Locate every Plasmodium parasite and every leukocyte.
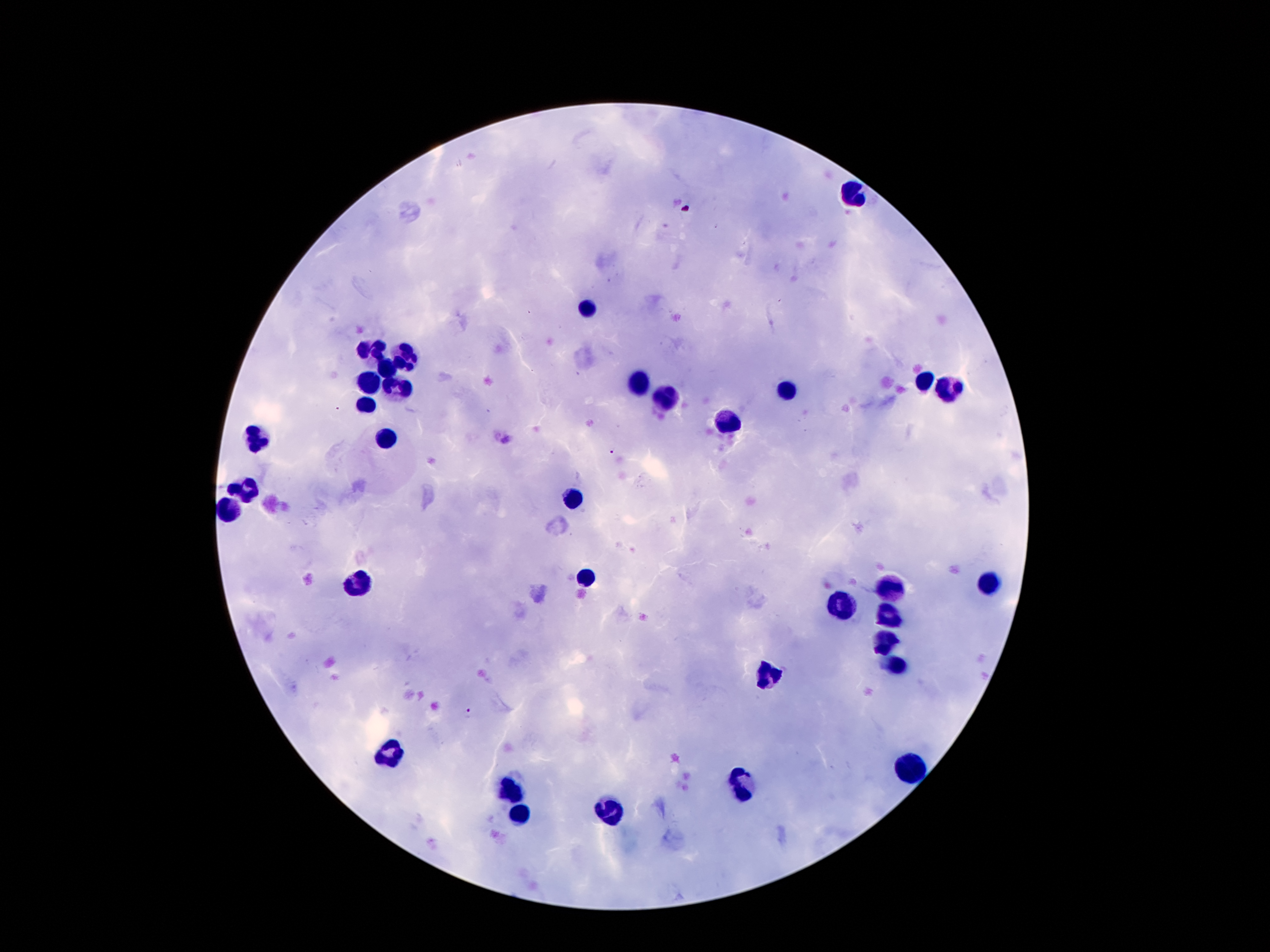

Approximate object centers, in pixels from the top-left corner.
Plasmodium parasites: (x=613, y=451), (x=466, y=712).
Leukocytes: (x=854, y=192), (x=587, y=307), (x=373, y=352), (x=409, y=357), (x=389, y=366), (x=925, y=380), (x=368, y=383), (x=637, y=383), (x=394, y=389), (x=948, y=391), (x=791, y=392), (x=666, y=399), (x=366, y=407), (x=730, y=421), (x=253, y=439), (x=384, y=439), (x=246, y=487), (x=575, y=498), (x=232, y=505), (x=587, y=576), (x=360, y=580), (x=988, y=582), (x=891, y=589), (x=839, y=608), (x=888, y=617), (x=884, y=644), (x=898, y=664), (x=766, y=675), (x=391, y=752), (x=911, y=767), (x=739, y=789), (x=514, y=792), (x=609, y=813), (x=519, y=816).

Summary:
  - Stain: Giemsa
  - Magnification: 100x
  - Field of view: one from this slide
  - Capture: smartphone camera through the microscope eyepiece
  - Patient malaria status: positive for Plasmodium falciparum
  - Preparation: thick blood smear
  - Image size: 1270×952 pixels